Assess this cell for malaria.
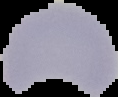

Uninfected.

image type = segmented cell region with the area outside set to black
image size = 118×97 pixels
preparation = thin blood smear